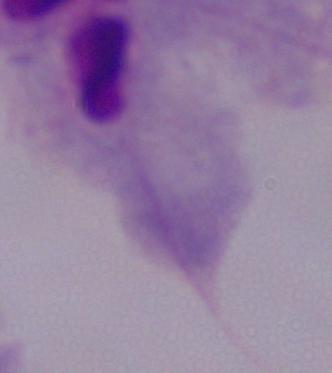
Micrograph. Captured at 1000x magnification. A trichomonad is seen.